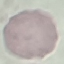 Result: no malaria parasites seen. Photographed with a smartphone camera at the microscope eyepiece. Giemsa stain. Thin blood film. Automatically extracted cell patch, resized to 64 × 64 pixels.